Assess the morphology of the erythrocytes.
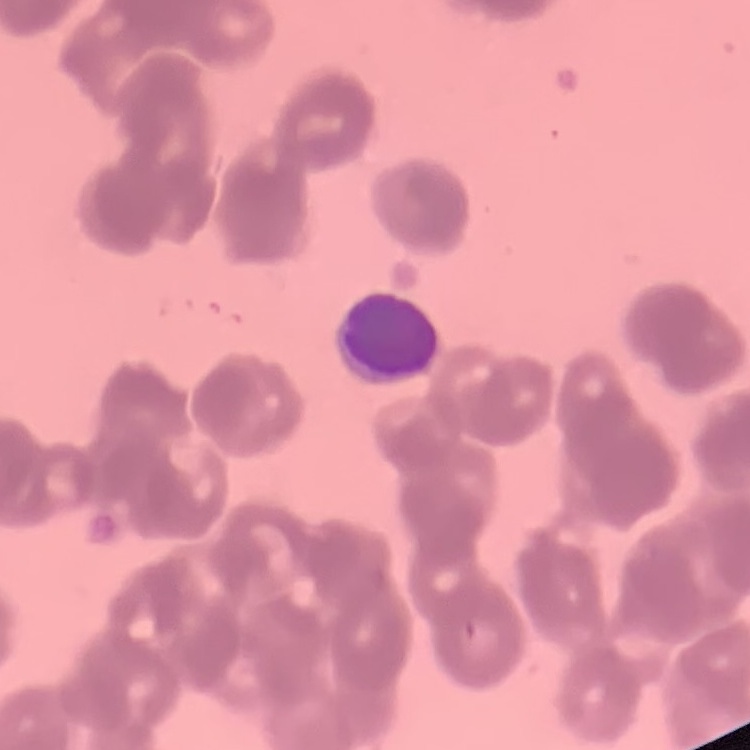
They show rouleaux formation.

One tile cut from a larger photomicrograph. Thin blood film. Stained with either Field's or Giemsa.